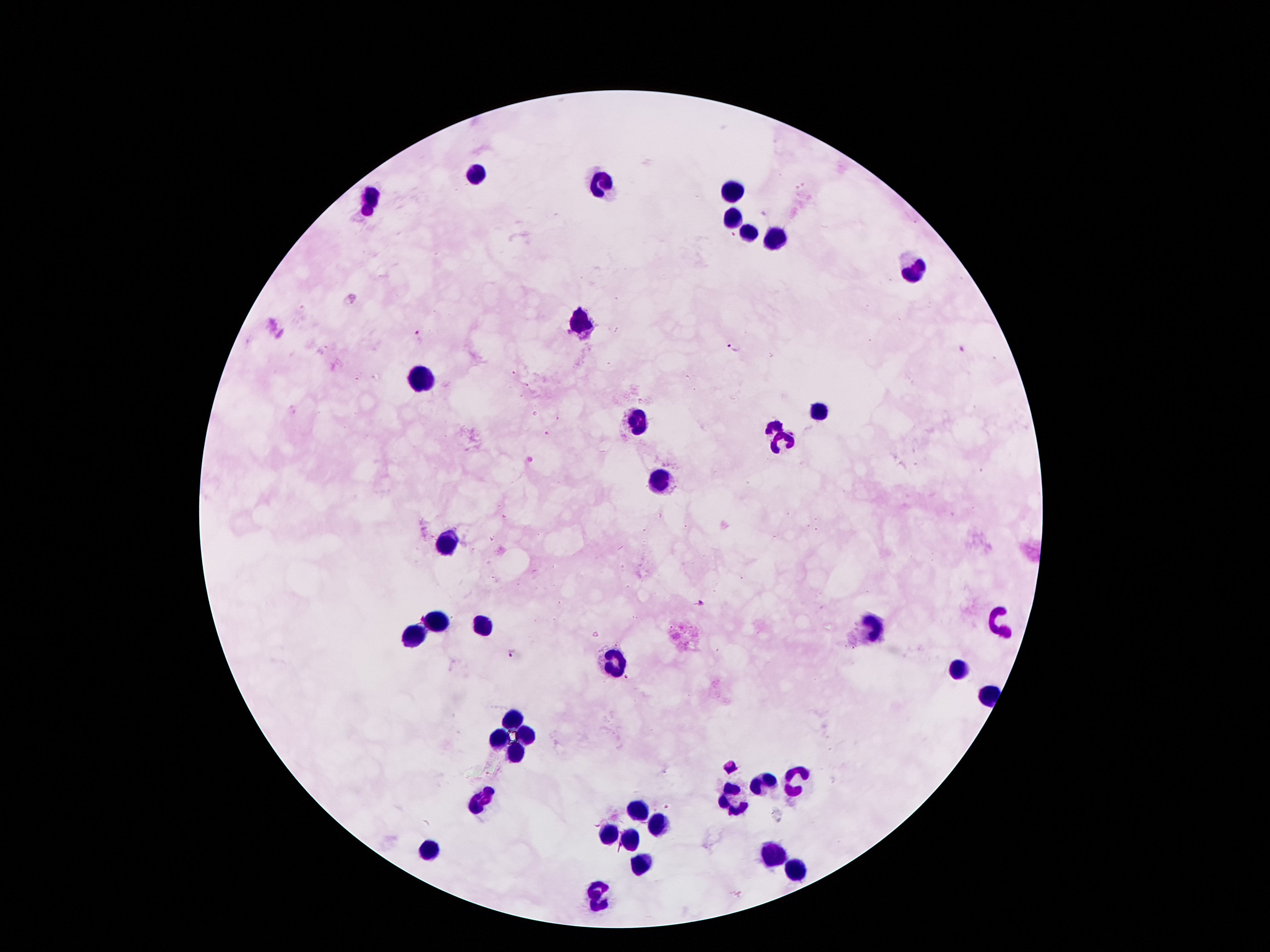
Approximate centers as [x, y] in pixels. Malaria parasite locations: [421, 336], [735, 348], [700, 604], [512, 654]. Leukocyte locations: [477, 175], [602, 183], [732, 191], [371, 198], [732, 221], [749, 232], [772, 239], [915, 269], [582, 325], [421, 380], [820, 412], [638, 422], [775, 426], [782, 445], [661, 480], [448, 543], [437, 623], [484, 625], [1001, 625], [874, 628], [414, 633], [616, 666], [958, 670], [990, 691], [516, 719], [527, 734], [498, 736], [513, 750], [797, 780], [763, 784], [732, 797], [482, 798], [638, 809], [657, 821], [607, 836], [630, 842], [430, 847], [772, 854], [641, 866], [795, 870], [600, 895]. Image is 1270×952 pixels. Giemsa stain. Smartphone photograph taken through the microscope eyepiece. Patient malaria status: infected with Plasmodium falciparum. 100x magnification. Thick blood film. Single field of view.